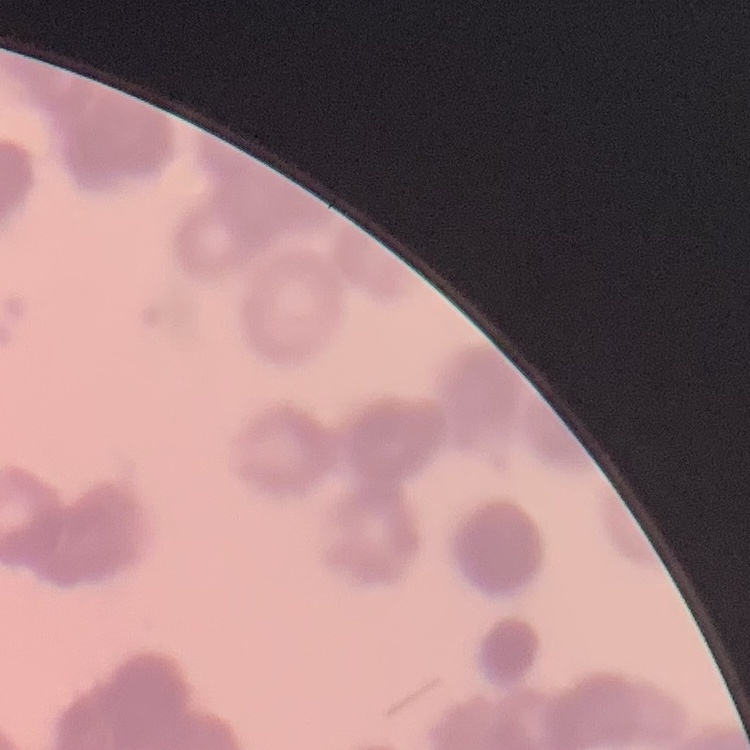 The erythrocytes show rouleaux formation. One tile cut from a larger photomicrograph. Field's or Giemsa stain. Thin blood smear.